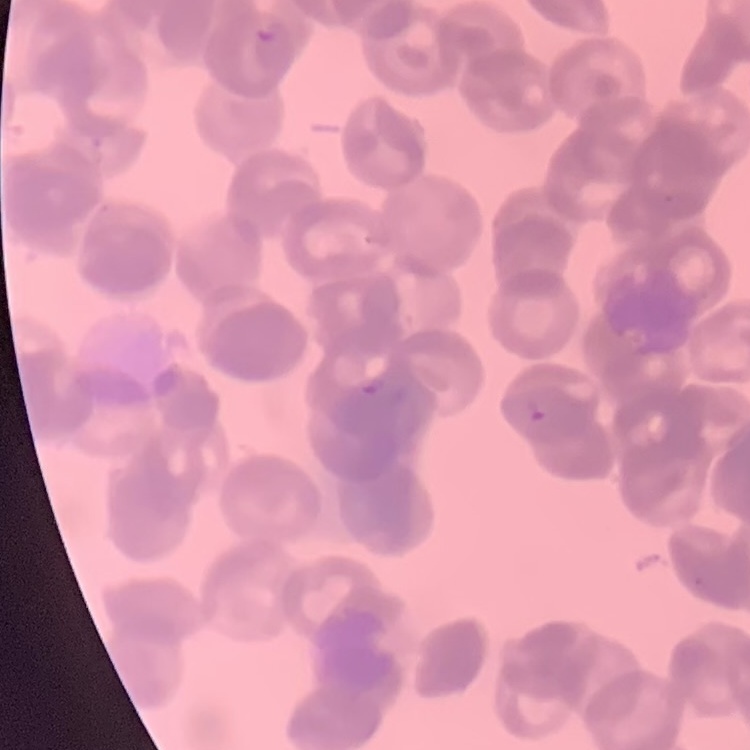
red_blood_cell_morphology: rouleaux formation
image_type: square crop of a larger photomicrograph
stain: Field's or Giemsa
preparation: thin peripheral smear